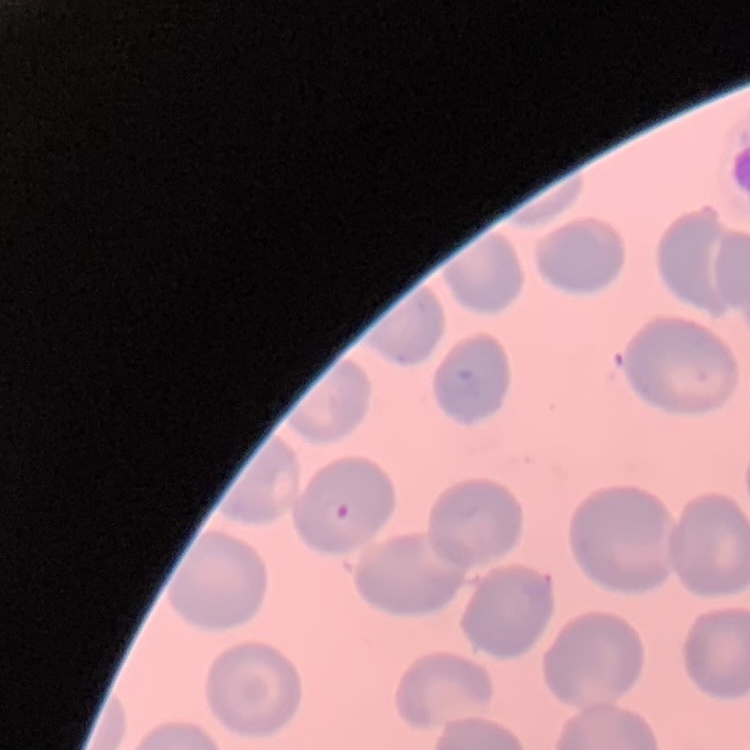

{
  "erythrocyte_morphology": "no rouleaux formation",
  "preparation": "thin blood smear",
  "image_type": "square crop of a larger photomicrograph",
  "stain": "Field's or Giemsa"
}